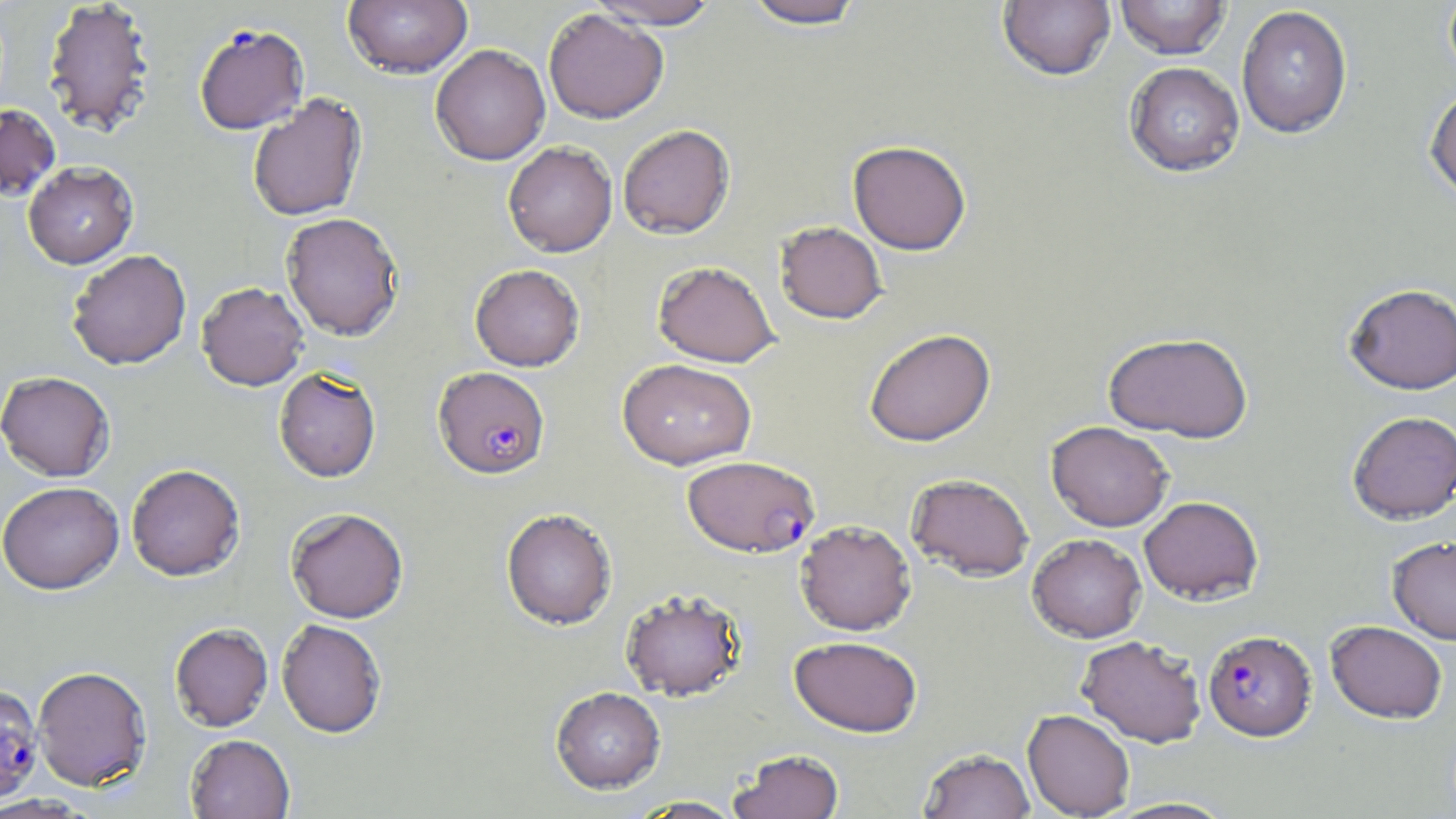

slide_level_diagnosis: Plasmodium falciparum
image_size: 1456×819 pixels
magnification: 1000x
plasmodium_falciparum_infected_red_blood_cell_locations: 'approximate bounding boxes as (x1, y1, x2, y2) in pixels: (193, 23, 310, 136), (433, 367, 550, 480), (681, 454, 819, 558), (1203, 629, 1316, 741), (0, 684, 43, 804)'
modality: optical microscopy
field_of_view: single
preparation: thin blood film
stain: May-Grünwald-Giemsa
uninfected_red_blood_cell_locations: 'approximate bounding boxes as (x1, y1, x2, y2) in pixels: (343, 0, 473, 78), (587, 0, 721, 29), (740, 0, 869, 29), (998, 0, 1116, 81), (1116, 0, 1231, 59), (1443, 0, 1456, 83), (41, 1, 157, 137), (1236, 5, 1353, 138), (543, 8, 668, 124), (430, 44, 550, 165), (1124, 61, 1245, 177), (1424, 84, 1456, 202), (247, 94, 367, 223), (0, 104, 61, 201), (618, 124, 735, 238), (848, 139, 971, 255), (503, 141, 617, 257), (23, 161, 138, 269), (280, 212, 404, 341), (775, 221, 888, 324), (66, 249, 192, 370), (652, 260, 780, 367), (470, 263, 585, 371), (196, 281, 309, 390), (1343, 282, 1456, 394), (864, 328, 996, 447), (1103, 331, 1254, 442), (617, 358, 757, 470), (274, 367, 381, 482), (0, 371, 115, 482), (1346, 411, 1456, 523), (1046, 421, 1173, 531), (126, 464, 245, 581), (906, 472, 1034, 581), (1, 481, 124, 595), (1139, 495, 1264, 604), (286, 507, 409, 623), (501, 508, 617, 630), (795, 519, 916, 635), (1027, 533, 1147, 643), (1387, 536, 1456, 644), (620, 588, 748, 702), (276, 619, 387, 738), (1325, 620, 1448, 723), (169, 623, 273, 732), (789, 635, 922, 737), (1076, 635, 1207, 747), (32, 665, 152, 791), (550, 686, 666, 794), (1022, 708, 1135, 818), (185, 734, 295, 818), (918, 748, 1035, 819), (729, 749, 845, 819), (630, 796, 747, 818), (1101, 796, 1239, 818)'